State which parasite is depicted.
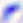
Toxoplasma gondii.

Summary:
  - Modality: micrograph
  - Magnification: 400x